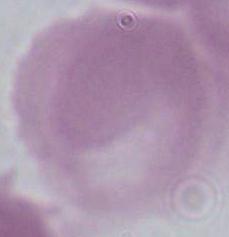
Summary:
  - Identification: erythrocyte
  - Magnification: 1000x
  - Modality: photomicrograph